Describe the morphology of the red blood cells.
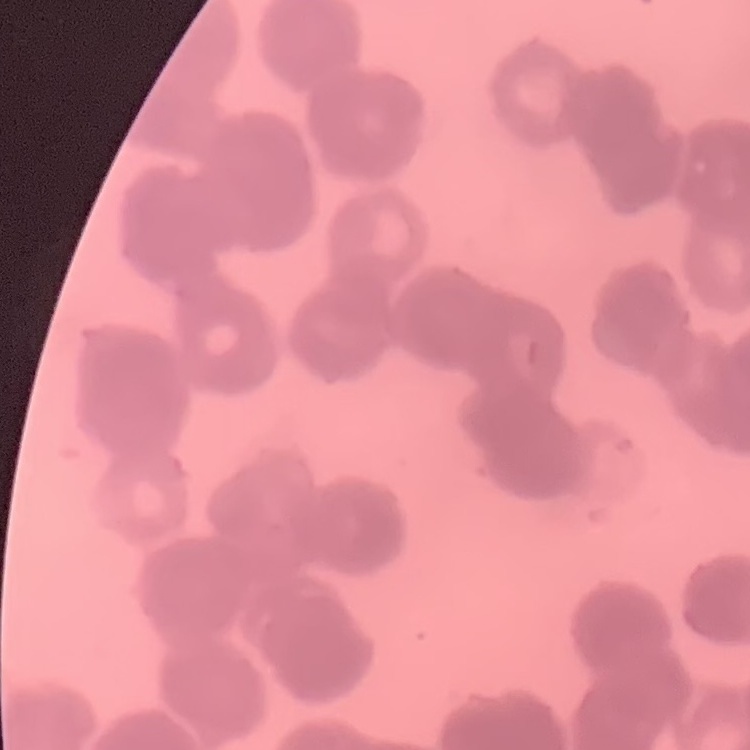
They show rouleaux formation.

Square crop of a larger photomicrograph. Field's or Giemsa stain. Thin peripheral smear.